State which parasite is depicted.
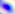

Toxoplasma gondii.

modality = micrograph
magnification = 400x